Outline each blood parasite and name the species.
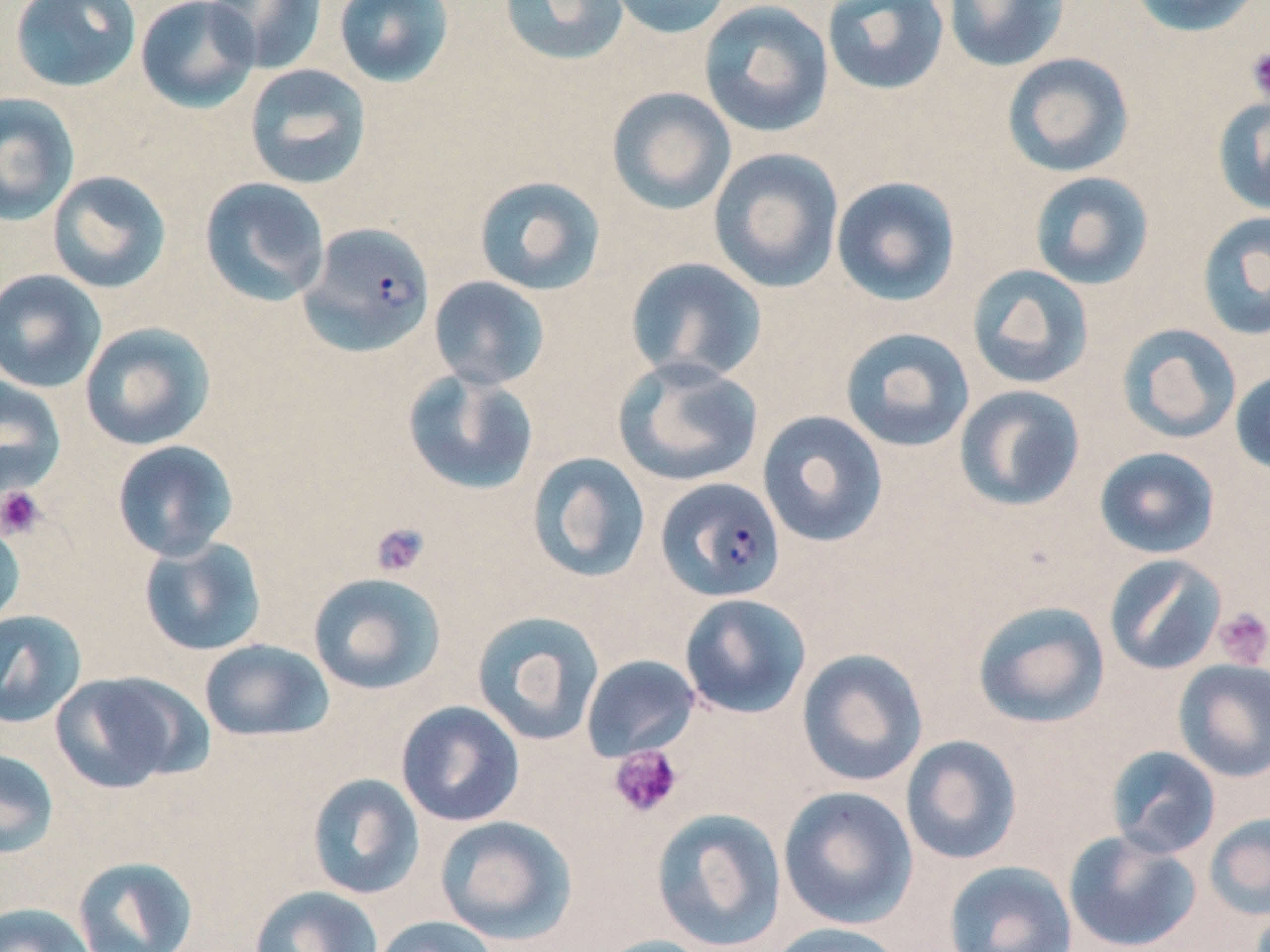

Approximate bounding boxes as [x1, y1, x2, y2] in pixels.
Plasmodium falciparum-infected red blood cells: [299, 221, 435, 357], [655, 477, 786, 603].
No Plasmodium ovale, Plasmodium malariae, Plasmodium vivax, Babesia divergens, or Trypanosoma brucei observed.

slide_level_diagnosis: Plasmodium falciparum
stain: May-Grünwald-Giemsa
preparation: thin blood smear
image_size: 1270×952 pixels
uninfected_red_blood_cell_locations: 'approximate bounding boxes as [x1, y1, x2, y2] in pixels: [135, 0, 261, 114], [204, 0, 328, 74], [333, 0, 455, 87], [499, 0, 631, 67], [605, 0, 735, 38], [822, 0, 950, 96], [942, 0, 1071, 73], [1126, 0, 1263, 37], [9, 1, 143, 91], [698, 1, 835, 138], [1002, 52, 1135, 178], [243, 64, 372, 189], [605, 86, 737, 215], [0, 92, 80, 226], [1212, 96, 1270, 216], [708, 147, 845, 294], [47, 170, 172, 294], [1029, 171, 1154, 291], [473, 175, 606, 295], [831, 175, 962, 306], [199, 177, 330, 307], [1196, 211, 1270, 341], [625, 257, 767, 384], [967, 264, 1095, 390], [0, 268, 107, 393], [428, 276, 550, 390], [79, 321, 216, 451], [1117, 323, 1242, 444], [839, 327, 975, 453], [613, 357, 765, 487], [1230, 368, 1270, 476], [402, 369, 540, 497], [0, 374, 66, 497], [954, 384, 1086, 512], [757, 409, 888, 548], [111, 439, 239, 562], [1094, 446, 1221, 559], [526, 452, 651, 583], [0, 517, 26, 629], [138, 536, 267, 657], [1103, 554, 1227, 675], [307, 572, 447, 695], [679, 593, 812, 719], [971, 600, 1111, 730], [0, 610, 87, 728], [472, 610, 605, 747], [199, 639, 334, 743], [795, 648, 929, 787], [581, 655, 700, 761], [1172, 658, 1270, 783], [50, 670, 202, 793], [396, 700, 525, 827], [900, 735, 1023, 865], [1105, 745, 1221, 859], [0, 748, 59, 859], [306, 773, 425, 899], [778, 785, 918, 929], [650, 807, 787, 951], [1204, 813, 1270, 921], [435, 815, 577, 945], [1063, 830, 1202, 952], [73, 855, 199, 952], [943, 860, 1078, 952], [249, 885, 383, 952], [0, 902, 97, 952], [371, 915, 500, 952], [766, 922, 908, 952], [590, 934, 719, 952]'
field_of_view: one of a larger specimen
modality: light microscopy
magnification: 1000x
platelet_locations: 'approximate bounding boxes as [x1, y1, x2, y2] in pixels: [1246, 47, 1270, 102], [0, 486, 46, 539], [370, 522, 430, 578], [1212, 606, 1270, 669], [608, 745, 683, 818]'